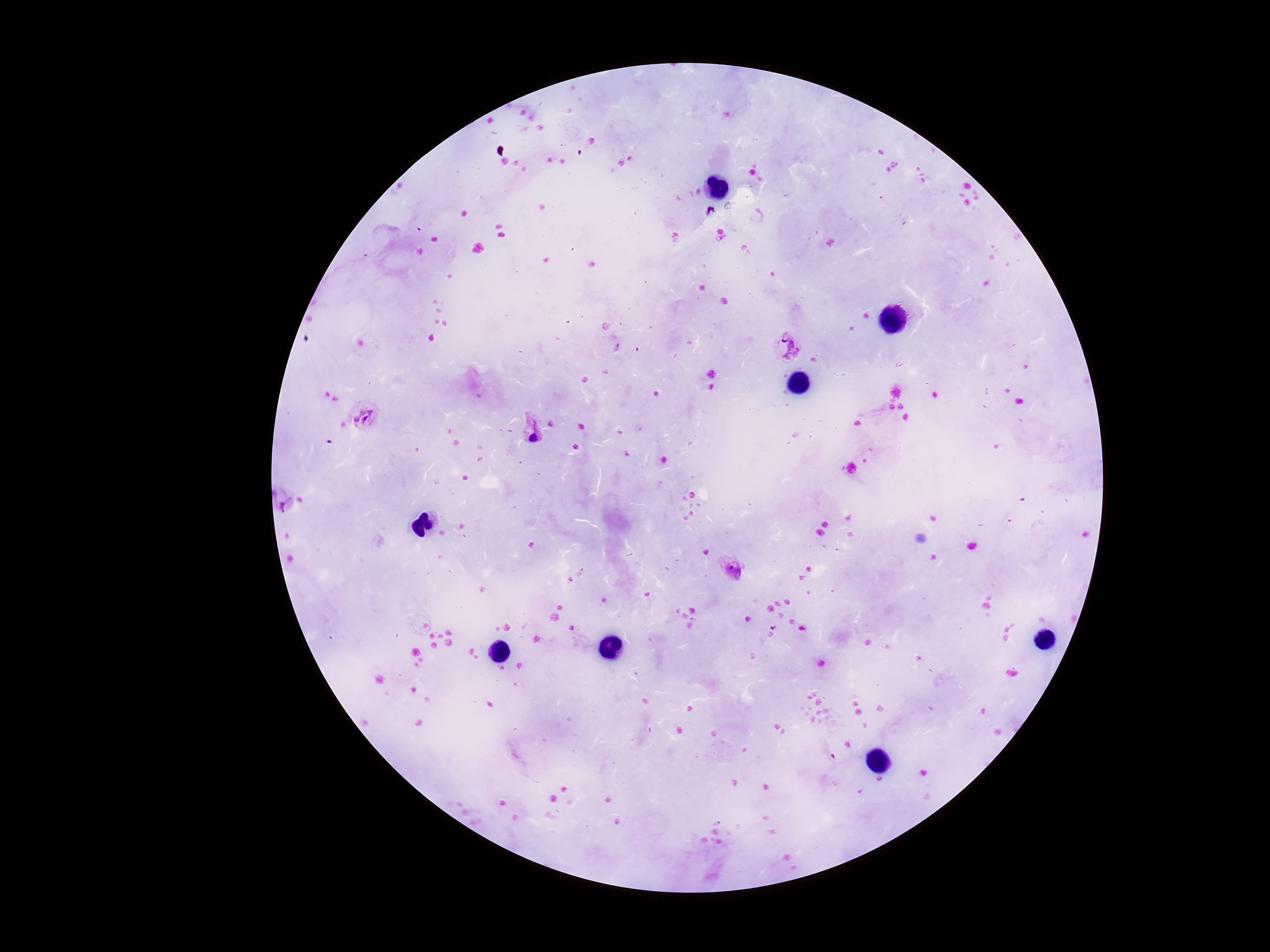
{
  "patient_malaria_status": "infected",
  "stain": "Giemsa",
  "field_of_view": "single",
  "capture": "smartphone camera through the microscope eyepiece",
  "image_size": "1270×952 pixels",
  "preparation": "thick peripheral-blood smear",
  "magnification": "100x",
  "plasmodium_parasite_locations": "approximate centers as {x, y} in pixels: {785, 346}, {366, 416}, {532, 433}, {281, 500}, {732, 570}"
}